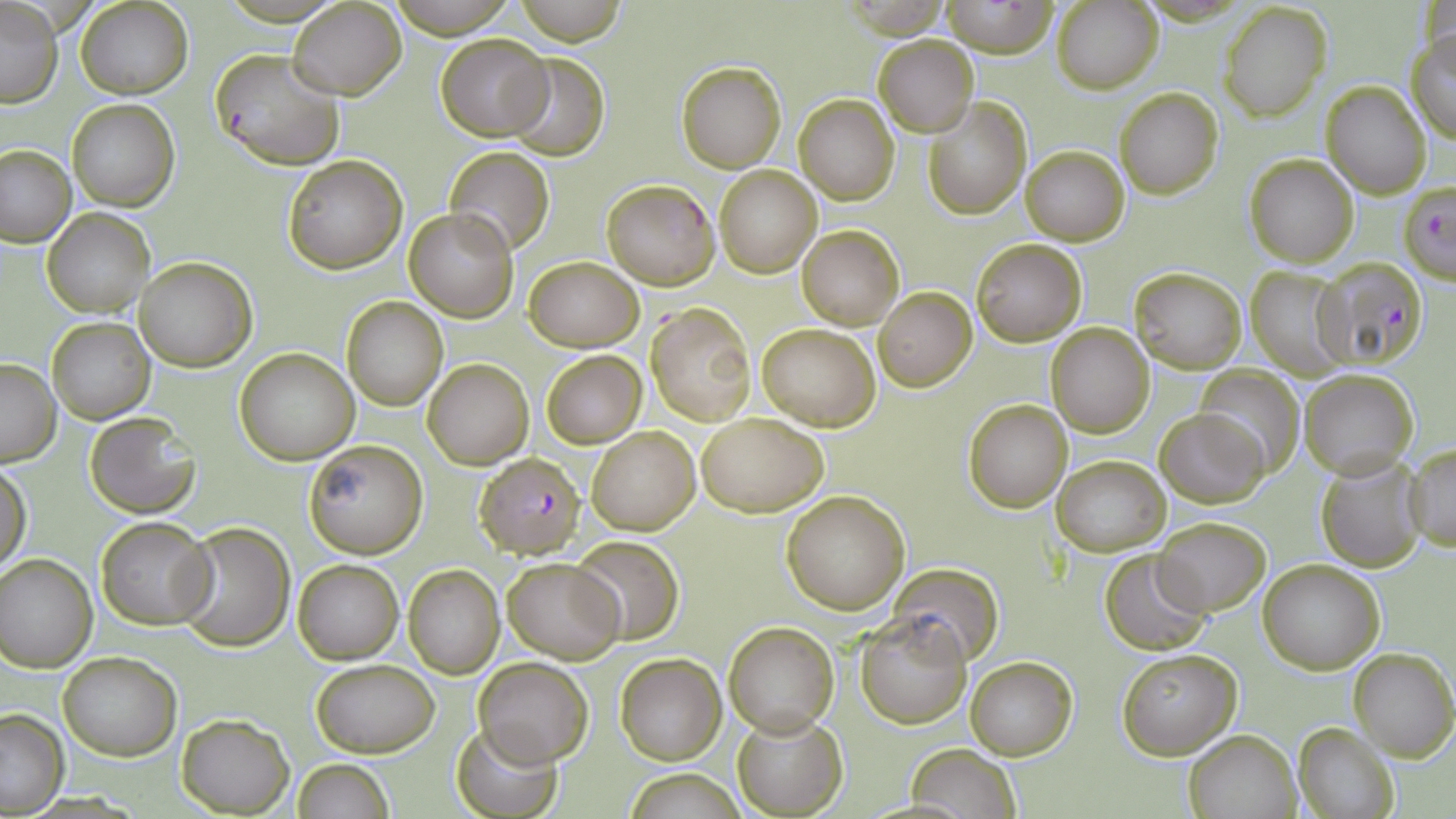

Summary:
  - Coordinate format: approximate bounding boxes as (x1,y1)-(x2,y2) corner pairs in pixels
  - Plasmodium falciparum-infected red blood cell locations: (210,49)-(347,172), (602,178)-(719,290), (1398,180)-(1456,286), (1315,257)-(1429,370), (473,450)-(585,557)
  - Uninfected red blood cell locations: (383,0)-(520,37), (513,0)-(626,45), (940,0)-(1060,58), (74,1)-(193,100), (1053,1)-(1163,93), (1,2)-(63,109), (289,2)-(407,98), (1217,2)-(1333,122), (1407,29)-(1456,145), (436,34)-(553,141), (873,35)-(978,136), (504,51)-(610,161), (677,61)-(786,172), (1321,81)-(1431,200), (1115,87)-(1224,199), (794,94)-(900,205), (67,99)-(179,211), (924,99)-(1031,220), (0,143)-(75,247), (444,145)-(555,255), (1021,145)-(1129,245), (1245,154)-(1360,268), (281,155)-(407,274), (714,167)-(822,278), (42,208)-(153,317), (404,208)-(518,322), (796,224)-(904,330), (971,239)-(1086,346), (524,255)-(642,352), (134,256)-(256,371), (1129,267)-(1247,374), (1245,267)-(1350,376), (874,287)-(976,391), (341,295)-(448,411), (646,302)-(756,426), (47,316)-(155,425), (1046,322)-(1155,438), (757,323)-(881,431), (235,348)-(360,464), (542,351)-(646,447), (423,357)-(534,470), (0,359)-(61,467), (1193,365)-(1306,479), (1297,368)-(1419,479), (963,399)-(1072,512), (1155,408)-(1268,509), (696,412)-(828,517), (83,414)-(200,519), (587,427)-(700,535), (302,439)-(429,559), (1405,442)-(1456,550), (1053,455)-(1172,555), (1315,455)-(1425,572), (1,458)-(32,571), (781,489)-(911,614), (95,516)-(216,629), (1155,517)-(1271,616), (173,522)-(295,652), (571,536)-(685,643), (1099,549)-(1211,655), (0,553)-(98,671), (503,557)-(626,664), (294,558)-(403,664), (1258,559)-(1383,674), (889,563)-(1004,666), (404,565)-(505,679), (855,612)-(972,729), (722,620)-(839,737), (1349,647)-(1455,763), (1115,648)-(1243,760), (57,650)-(181,761), (614,652)-(726,765), (966,655)-(1079,761), (311,657)-(439,757), (473,657)-(592,767), (0,708)-(69,814), (733,710)-(846,816), (177,713)-(294,816), (448,720)-(564,819), (1293,721)-(1401,819), (1184,728)-(1302,819), (907,744)-(1021,819), (291,757)-(396,819), (620,769)-(748,818)
  - Slide-level diagnosis: Plasmodium falciparum
  - Preparation: thin blood film
  - Stain: May-Grünwald-Giemsa
  - Magnification: 1000x
  - Image size: 1456×819 pixels
  - Modality: light microscopy
  - Field of view: one of a larger specimen